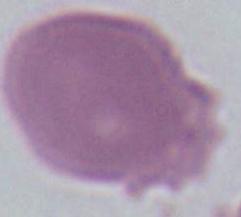 Micrograph. 1000x magnification. An erythrocyte is seen.